State the blood parasite species.
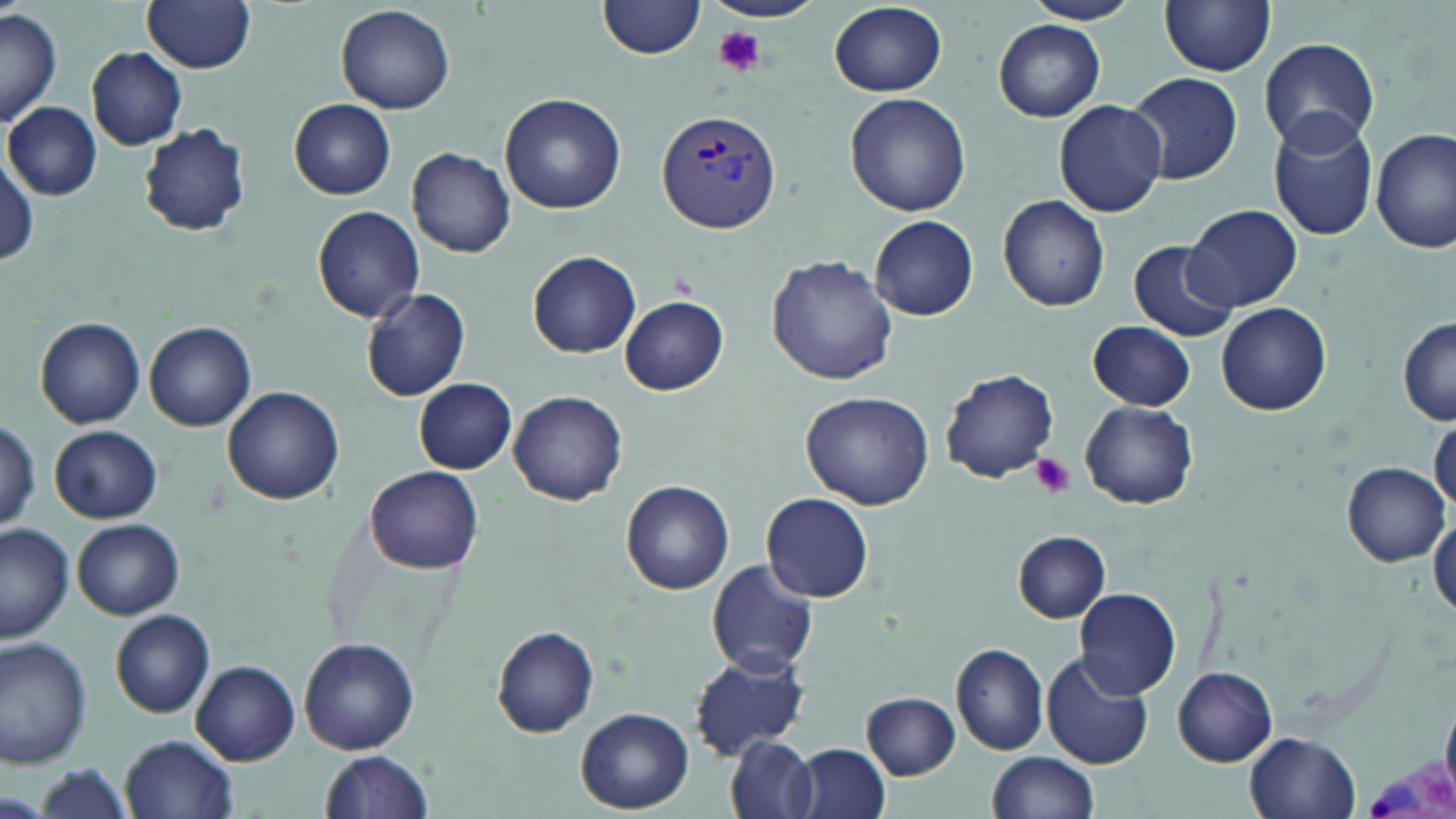
Plasmodium vivax.

Summary:
  - Coordinate format: approximate bounding boxes as named x1/y1/x2/y2 corners in pixels
  - Platelet locations: (x1=711, y1=26, x2=766, y2=77), (x1=1031, y1=453, x2=1074, y2=497)
  - Plasmodium vivax-infected red blood cell locations: (x1=657, y1=108, x2=781, y2=234), (x1=1367, y1=744, x2=1454, y2=819)
  - Uninfected red blood cell locations: (x1=143, y1=0, x2=258, y2=73), (x1=600, y1=0, x2=706, y2=58), (x1=705, y1=0, x2=825, y2=23), (x1=1020, y1=0, x2=1143, y2=25), (x1=1160, y1=0, x2=1277, y2=75), (x1=336, y1=3, x2=455, y2=114), (x1=827, y1=3, x2=947, y2=96), (x1=1, y1=8, x2=62, y2=126), (x1=994, y1=20, x2=1106, y2=120), (x1=1257, y1=37, x2=1380, y2=152), (x1=86, y1=47, x2=188, y2=150), (x1=1127, y1=71, x2=1241, y2=185), (x1=844, y1=92, x2=972, y2=216), (x1=499, y1=94, x2=625, y2=213), (x1=288, y1=99, x2=397, y2=199), (x1=1054, y1=100, x2=1167, y2=217), (x1=4, y1=102, x2=101, y2=199), (x1=1266, y1=114, x2=1380, y2=240), (x1=138, y1=123, x2=252, y2=236), (x1=1373, y1=129, x2=1453, y2=254), (x1=408, y1=146, x2=516, y2=257), (x1=1, y1=156, x2=40, y2=266), (x1=997, y1=195, x2=1110, y2=311), (x1=1186, y1=205, x2=1301, y2=312), (x1=312, y1=206, x2=424, y2=323), (x1=870, y1=215, x2=978, y2=320), (x1=1126, y1=239, x2=1241, y2=340), (x1=527, y1=251, x2=641, y2=357), (x1=767, y1=255, x2=897, y2=385), (x1=359, y1=286, x2=470, y2=401), (x1=619, y1=295, x2=730, y2=395), (x1=1217, y1=303, x2=1331, y2=416), (x1=1397, y1=316, x2=1456, y2=425), (x1=36, y1=319, x2=145, y2=428), (x1=1087, y1=321, x2=1195, y2=411), (x1=145, y1=324, x2=255, y2=430), (x1=941, y1=368, x2=1060, y2=484), (x1=414, y1=379, x2=517, y2=474), (x1=223, y1=386, x2=344, y2=505), (x1=510, y1=391, x2=628, y2=505), (x1=800, y1=392, x2=934, y2=509), (x1=1079, y1=401, x2=1198, y2=509), (x1=1429, y1=417, x2=1456, y2=514), (x1=0, y1=418, x2=42, y2=532), (x1=50, y1=425, x2=162, y2=522), (x1=1342, y1=462, x2=1448, y2=565), (x1=367, y1=465, x2=484, y2=573), (x1=622, y1=480, x2=734, y2=595), (x1=761, y1=493, x2=875, y2=603), (x1=1429, y1=511, x2=1456, y2=621), (x1=72, y1=518, x2=185, y2=619), (x1=0, y1=523, x2=76, y2=642), (x1=1013, y1=531, x2=1109, y2=622), (x1=706, y1=558, x2=818, y2=677), (x1=1076, y1=588, x2=1181, y2=698), (x1=111, y1=611, x2=214, y2=718), (x1=494, y1=625, x2=600, y2=736), (x1=299, y1=637, x2=419, y2=754), (x1=0, y1=638, x2=92, y2=770), (x1=952, y1=645, x2=1047, y2=756), (x1=691, y1=651, x2=812, y2=758), (x1=1041, y1=653, x2=1156, y2=769), (x1=193, y1=661, x2=298, y2=763), (x1=1173, y1=667, x2=1278, y2=765), (x1=863, y1=692, x2=960, y2=779), (x1=577, y1=708, x2=693, y2=812), (x1=1246, y1=732, x2=1360, y2=818), (x1=121, y1=734, x2=239, y2=818), (x1=726, y1=736, x2=817, y2=818), (x1=793, y1=744, x2=892, y2=819), (x1=319, y1=751, x2=434, y2=818), (x1=986, y1=752, x2=1099, y2=819), (x1=31, y1=765, x2=140, y2=819), (x1=0, y1=792, x2=49, y2=817)
  - Field of view: single
  - Image size: 1456×819 pixels
  - Magnification: 1000x
  - Stain: May-Grünwald-Giemsa
  - Preparation: thin blood smear
  - Modality: light microscopy